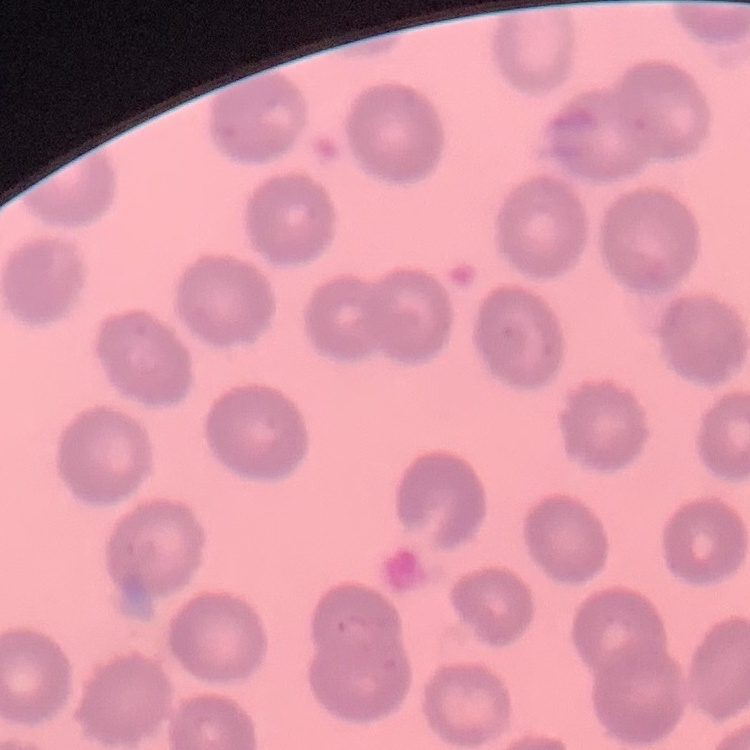 The erythrocytes show no rouleaux formation. Thin peripheral smear. One tile cut from a larger photomicrograph. Stained with either Field's or Giemsa.